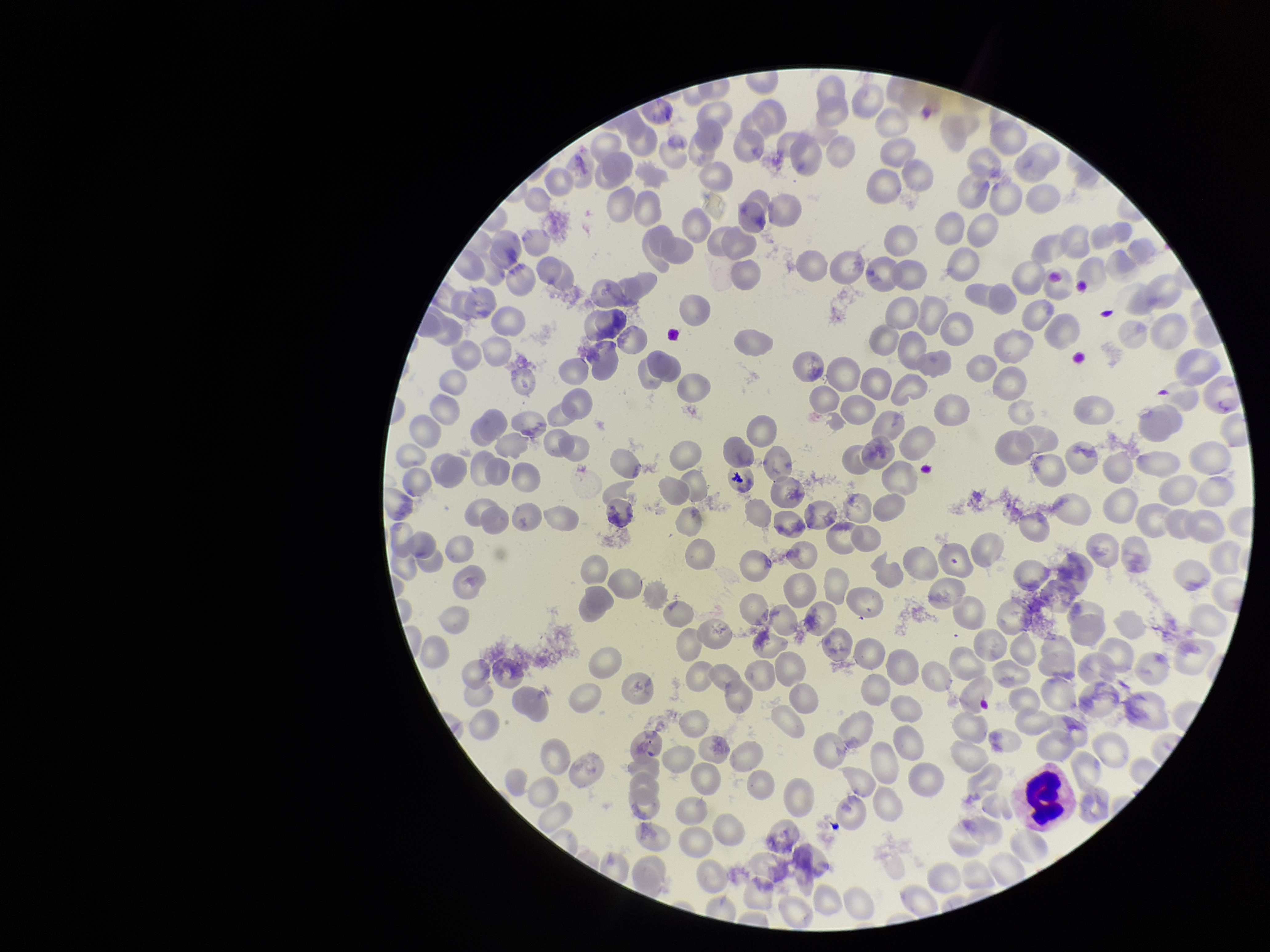

image size = 1270×952 pixels
stain = Giemsa
species reported for this patient = Plasmodium falciparum
capture = smartphone photograph through the microscope eyepiece
patient malaria status = infected
parasitized red blood cell count = 0
preparation = thin smear
red blood cell count = 225
field of view = single
parasitized red blood cells = none detected